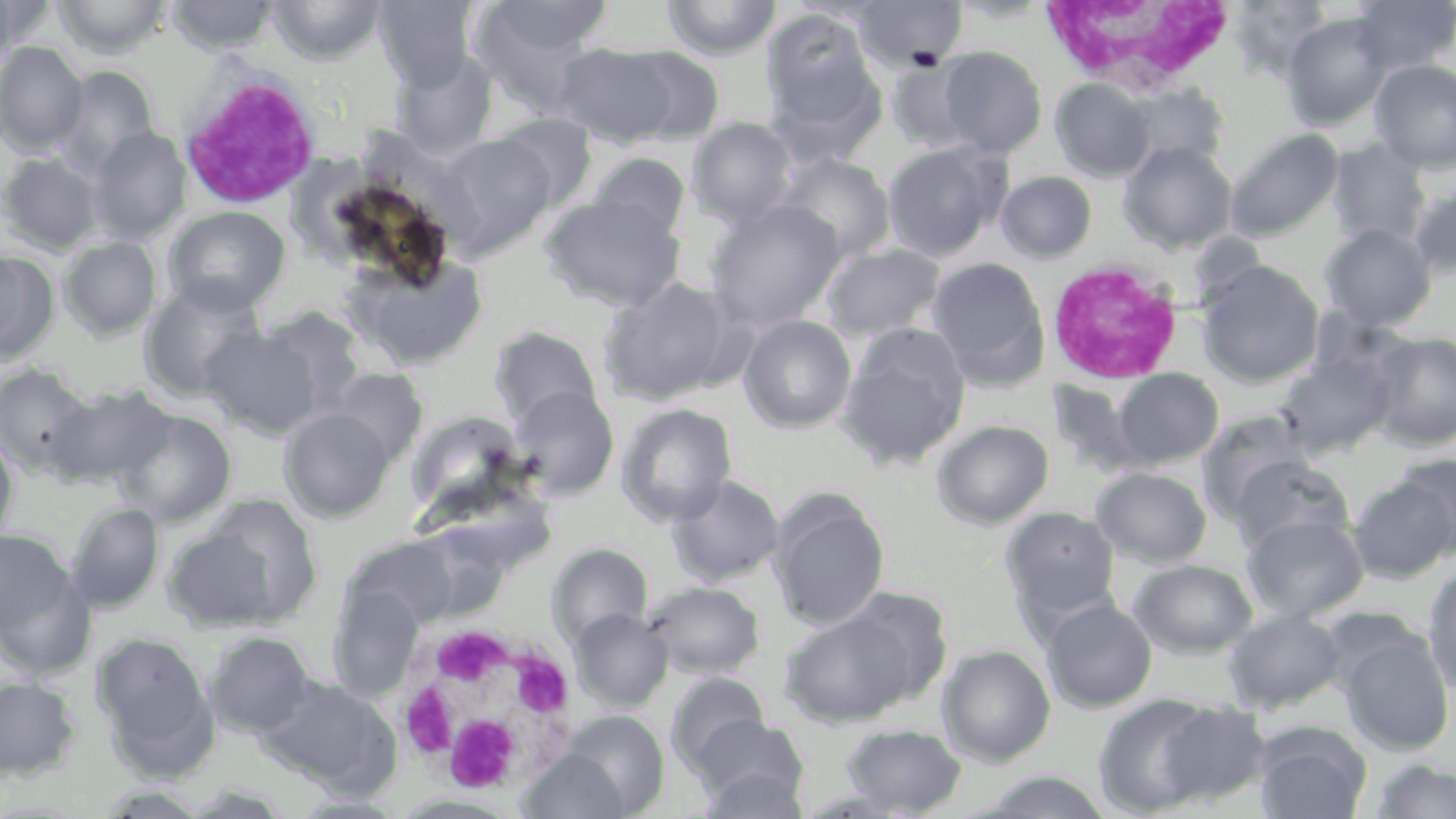
Approximate bounding boxes as (x1,y1)-(x2,y2) corner pairs in pixels. Uninfected red blood cell locations: (0,0)-(54,59), (52,0)-(172,58), (167,0)-(280,55), (268,0)-(386,64), (470,0)-(610,113), (662,0)-(782,59), (852,0)-(968,74), (1350,0)-(1455,75), (372,1)-(477,90), (1230,1)-(1335,76), (759,9)-(886,149), (1282,13)-(1394,130), (0,41)-(88,156), (553,43)-(680,148), (619,46)-(725,145), (936,47)-(1047,158), (390,50)-(499,158), (887,55)-(985,153), (1370,59)-(1456,171), (54,66)-(159,175), (1051,79)-(1155,182), (1117,83)-(1229,175), (494,112)-(597,212), (687,117)-(798,226), (88,126)-(191,243), (1226,128)-(1343,241), (434,134)-(554,259), (1327,139)-(1431,247), (882,141)-(1010,261), (1120,141)-(1237,254), (0,152)-(104,254), (588,152)-(691,241), (775,152)-(896,262), (996,171)-(1097,262), (1409,182)-(1456,278), (541,194)-(686,312), (705,198)-(846,330), (164,206)-(290,313), (1320,224)-(1437,331), (59,236)-(161,341), (821,243)-(946,341), (0,249)-(60,365), (344,254)-(489,371), (927,257)-(1050,387), (1196,260)-(1325,388), (598,277)-(741,406), (140,278)-(268,400), (257,306)-(368,417), (739,314)-(857,433), (837,323)-(972,469), (203,325)-(323,437), (489,326)-(603,430), (1368,331)-(1456,450), (1275,345)-(1403,458), (0,363)-(95,478), (1110,367)-(1225,470), (327,369)-(429,467), (45,384)-(175,490), (509,386)-(620,499), (511,391)-(735,513), (617,402)-(738,525), (280,407)-(394,521), (114,408)-(237,528), (406,411)-(530,519), (1196,411)-(1317,522), (932,419)-(1054,529), (0,432)-(19,544), (1389,453)-(1456,560), (1229,454)-(1355,553), (1091,466)-(1213,567), (1348,474)-(1454,584), (667,475)-(785,586), (769,493)-(889,631), (66,502)-(164,612), (164,505)-(311,633), (1000,506)-(1121,623), (1242,513)-(1369,622), (0,528)-(73,635), (548,543)-(652,646), (1128,558)-(1258,658), (0,562)-(96,681), (1423,566)-(1456,698), (643,581)-(765,679), (1041,598)-(1157,712), (779,601)-(932,729), (571,608)-(673,710), (1224,608)-(1347,713), (1337,628)-(1454,756), (93,632)-(216,766), (205,632)-(316,738), (938,644)-(1056,766), (667,672)-(770,771), (0,676)-(81,779), (257,676)-(401,792), (1092,692)-(1223,816), (1154,700)-(1271,808), (543,710)-(670,818), (691,714)-(809,810), (840,723)-(966,815), (1253,725)-(1372,819), (518,747)-(639,819), (1369,759)-(1456,818), (698,764)-(808,819), (975,770)-(1115,818), (390,794)-(522,818), (291,796)-(409,817). White blood cell locations: (1039,2)-(1239,100), (181,63)-(324,199), (1050,261)-(1184,387), (392,620)-(581,794). Slide-level diagnosis: no evidence of blood parasites. One field of a larger specimen. 1000x magnification. May-Grünwald-Giemsa stain. Thin blood smear. Optical microscopy. Image is 1456×819 pixels.